Point out each leukocyte.
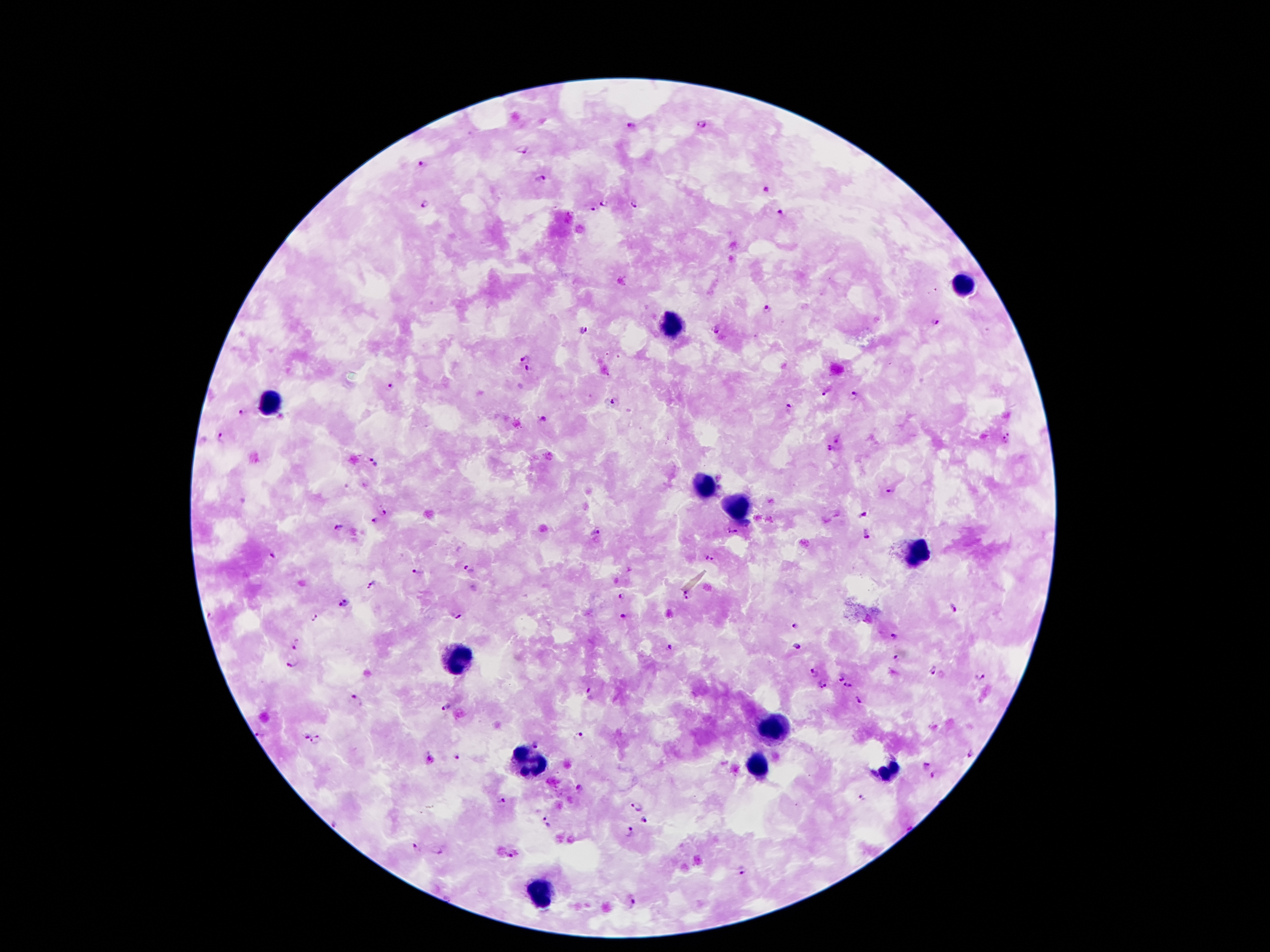

Approximate centers as (x, y) in pixels.
Leukocytes: (966, 279), (674, 326), (271, 401), (706, 487), (739, 508), (916, 555), (460, 656), (771, 731), (527, 762), (888, 765), (756, 770), (540, 889).

Malaria parasite locations: (701, 126), (633, 127), (521, 151), (420, 164), (542, 179), (768, 189), (425, 204), (605, 204), (634, 205), (591, 208), (782, 215), (768, 310), (934, 321), (718, 330), (583, 331), (523, 358), (528, 370), (391, 386), (825, 393), (854, 396), (614, 401), (789, 411), (242, 413), (544, 421), (1005, 437), (221, 438), (839, 438), (832, 450), (374, 461), (889, 492), (384, 511), (864, 515), (376, 522), (337, 528), (598, 533), (731, 533), (867, 534), (272, 556), (709, 559), (630, 568), (468, 570), (418, 572), (373, 582), (686, 595), (622, 597), (342, 604), (954, 608), (316, 617), (454, 617), (624, 617), (795, 626), (894, 636), (796, 647), (297, 648), (668, 648), (897, 658), (294, 665), (933, 671), (816, 673), (981, 677), (840, 678), (848, 684), (823, 685), (589, 689), (356, 701), (859, 701), (446, 708), (578, 735), (261, 736), (306, 736), (317, 741), (535, 743), (971, 754), (458, 757), (925, 764), (932, 775), (580, 788), (862, 798), (502, 802), (638, 806), (644, 821), (546, 823), (335, 824), (628, 833), (415, 848), (437, 852), (513, 854), (742, 870), (634, 901). Smartphone photograph taken through the microscope eyepiece. Patient malaria status: positive for Plasmodium falciparum. Image is 1270×952 pixels. Giemsa stain. Thick blood film. 100x magnification. One field from this slide.